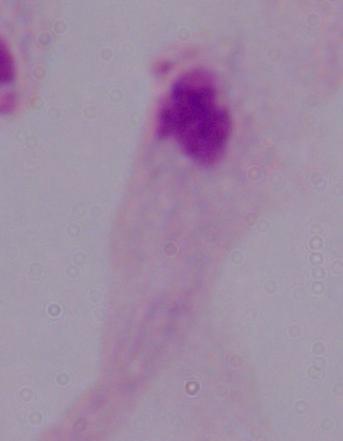
Summary:
  - Magnification: 1000x
  - Modality: photomicrograph
  - Identification: trichomonad